Evaluate for Plasmodium parasites.
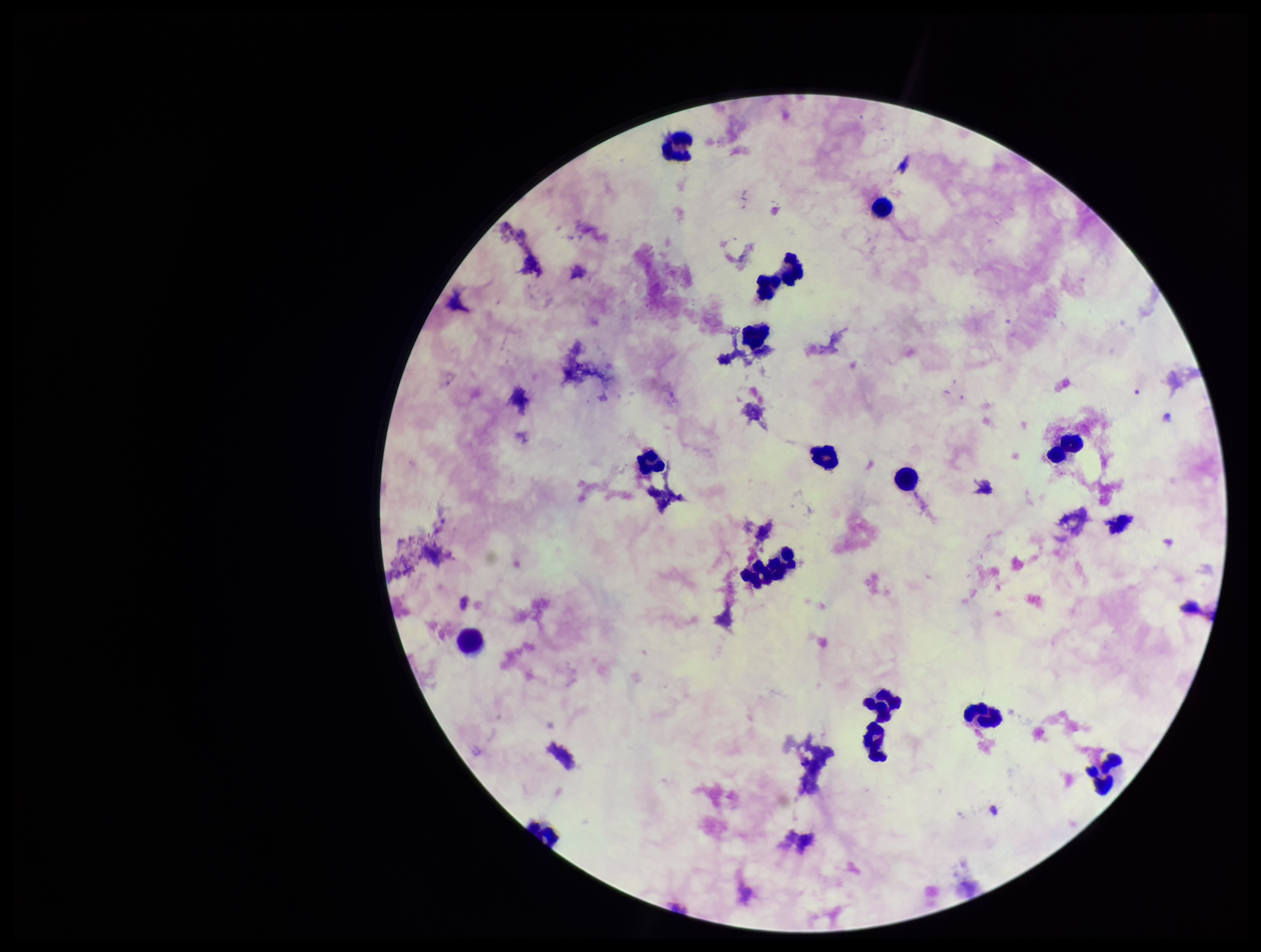
None identified.

stain = Giemsa
image size = 1261×952 pixels
preparation = thick smear
leukocyte count = 16
parasite count = 0
patient malaria status = negative
capture = smartphone photograph through the microscope eyepiece
field of view = one from this slide